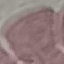

{
  "result": "no malaria parasites seen",
  "preparation": "thin blood smear",
  "image_type": "automatically extracted cell patch, resized to 64 × 64 pixels",
  "stain": "Giemsa",
  "capture": "smartphone through the microscope eyepiece"
}